Report the malaria status of this cell.
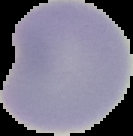
It is uninfected.

{
  "image_type": "cell region segmented out of the field of view; surrounding area masked to black",
  "image_size": "133×136 pixels",
  "preparation": "thin blood film"
}